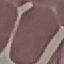 Malaria status: uninfected. Thin smear of blood. Giemsa-stained preparation. Acquired by smartphone through the microscope eyepiece. Automatically extracted cell patch, resized to 64 × 64 pixels.